Assess this cell for malaria.
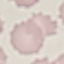

It is uninfected.

stain = Giemsa
capture = smartphone camera at the microscope eyepiece
image type = cell patch, automatically extracted from a larger field of view and resized to 64 × 64 pixels
preparation = thin smear